Rate the background quality.
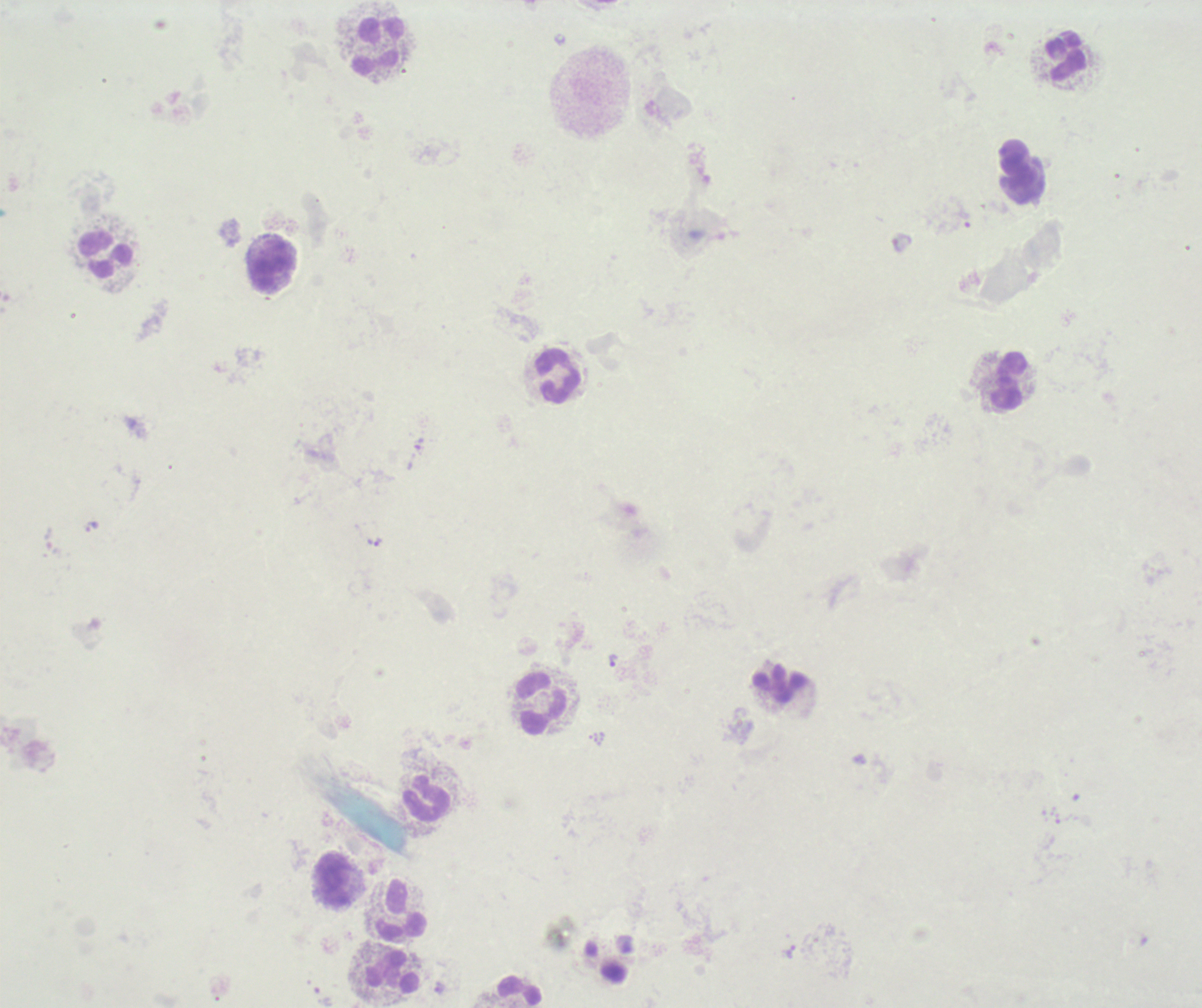

Poor.

Approximate centers as (x, y) in pixels.
Summary:
  - Trophozoite locations: (91, 526), (373, 541), (612, 660), (790, 952)
  - Leukocyte locations: (378, 45), (1065, 57), (106, 255), (270, 263), (558, 375), (1009, 380), (780, 683), (541, 702), (426, 799), (334, 878), (401, 910), (393, 972), (521, 990)
  - Preparation: thick smear of blood
  - Context: previously used in an actual diagnosis
  - Field of view: one from this slide
  - Image size: 1202×1008 pixels
  - Result: malaria parasites detected
  - Stain: Romanowsky
  - Magnification: 100x